Describe the morphology of the erythrocytes.
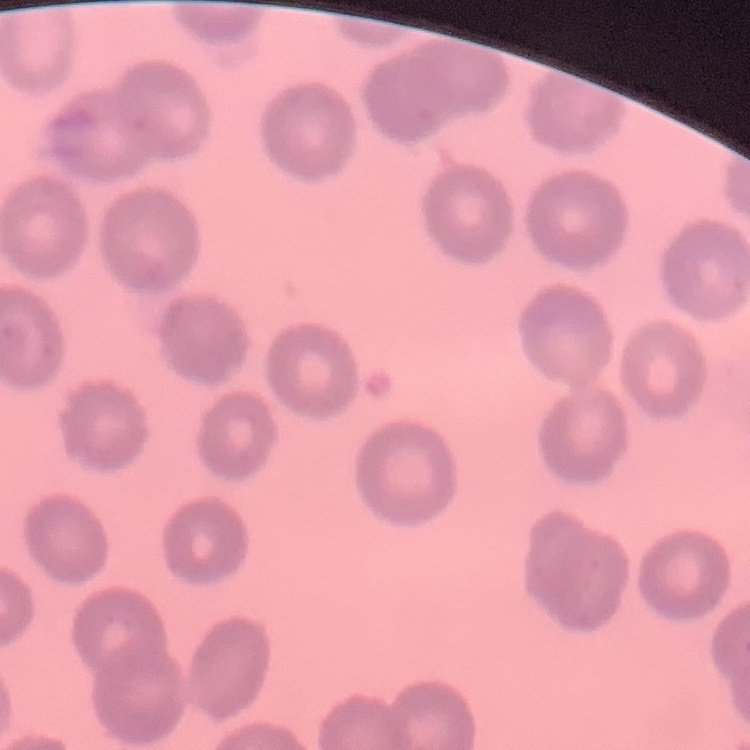
They show no rouleaux formation.

Summary:
  - Image type: square crop of a larger photomicrograph
  - Stain: Field's or Giemsa
  - Preparation: thin blood smear